Assess this cell for malaria.
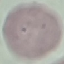

It is uninfected.

{
  "image_type": "cell patch, automatically extracted from a larger field of view and resized to 64 × 64 pixels",
  "preparation": "thin blood smear",
  "capture": "smartphone through the microscope eyepiece",
  "stain": "Giemsa"
}